State which cell type is depicted.
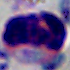
This is a leukocyte.

Summary:
  - Modality: micrograph
  - Magnification: 1000x